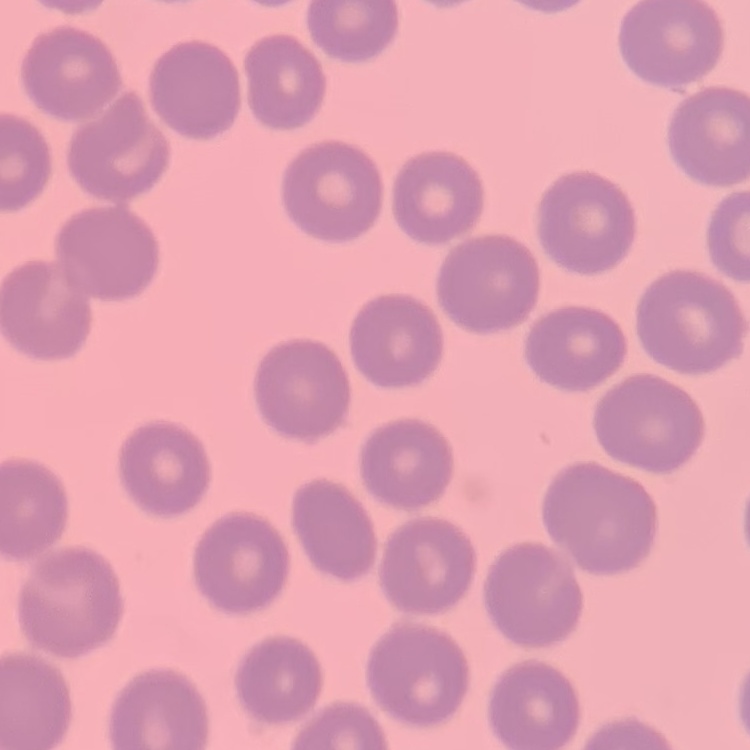
The erythrocytes show no rouleaux formation. Field's or Giemsa stain. One tile cut from a larger photomicrograph. Thin blood film.